Locate every Plasmodium falciparum-infected red blood cell.
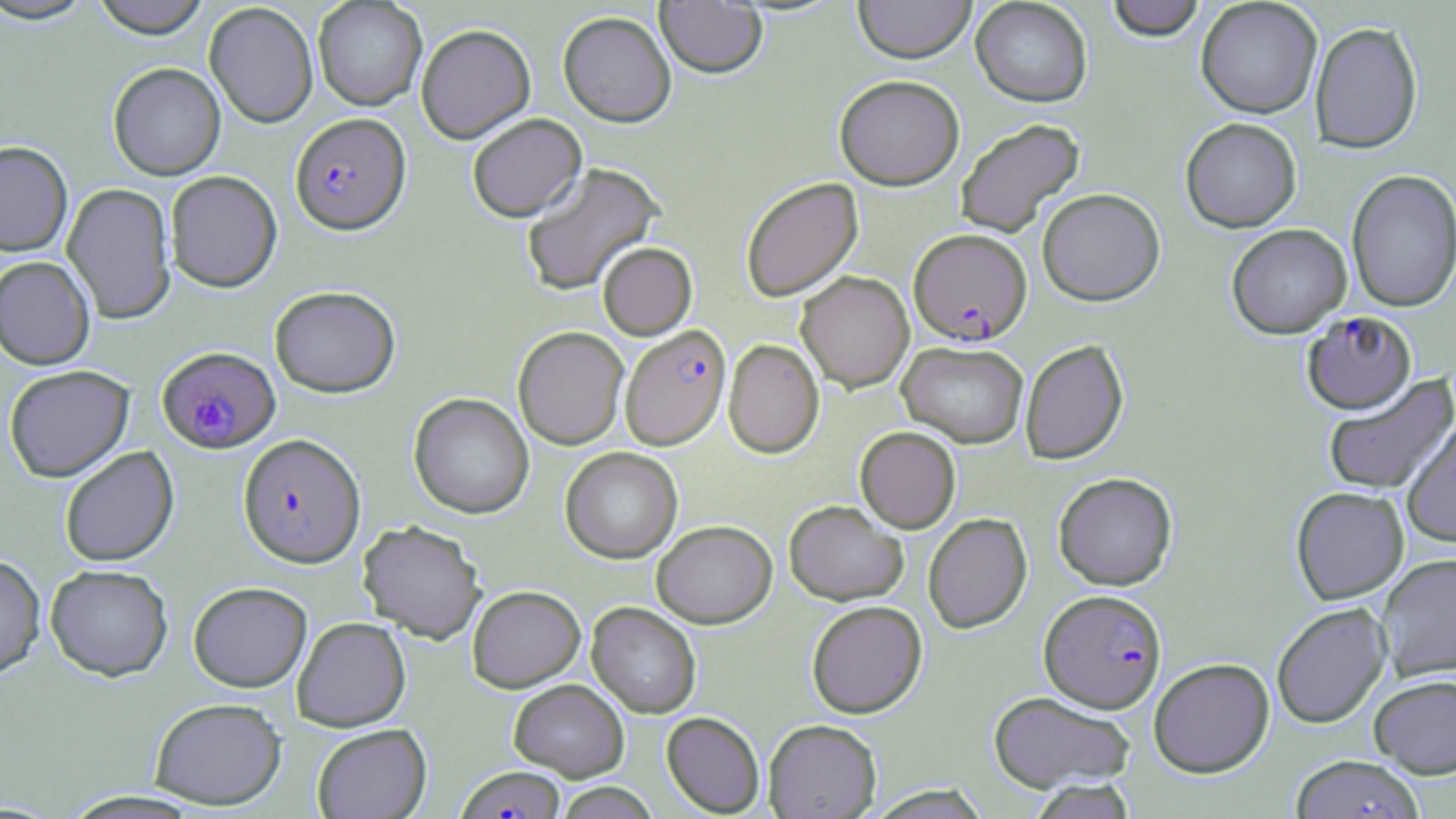

Approximate bounding boxes as [x1, y1, x2, y2] in pixels.
Plasmodium falciparum-infected red blood cells: [290, 112, 410, 234], [909, 228, 1032, 344], [1301, 311, 1417, 414], [619, 324, 731, 450], [157, 346, 280, 453], [238, 433, 365, 567], [1040, 588, 1167, 713], [456, 766, 566, 818].

slide-level diagnosis = Plasmodium falciparum
image size = 1456×819 pixels
preparation = thin blood smear
field of view = single
magnification = 1000x
uninfected red blood cell locations = approximate bounding boxes as [x1, y1, x2, y2] in pixels: [90, 0, 211, 38], [853, 0, 977, 63], [970, 0, 1092, 106], [1105, 0, 1206, 40], [1196, 0, 1322, 118], [0, 1, 98, 24], [313, 1, 427, 110], [655, 1, 767, 78], [204, 2, 318, 128], [557, 10, 676, 127], [1310, 20, 1423, 154], [416, 23, 536, 144], [108, 62, 226, 180], [834, 74, 964, 190], [467, 113, 586, 222], [955, 117, 1085, 238], [1180, 117, 1302, 232], [0, 141, 73, 256], [521, 162, 665, 296], [1346, 169, 1456, 312], [165, 170, 282, 292], [740, 177, 863, 302], [62, 182, 176, 324], [1037, 188, 1165, 305], [1226, 224, 1352, 338], [597, 242, 697, 340], [0, 255, 95, 370], [796, 271, 914, 392], [269, 285, 400, 397], [513, 326, 629, 449], [723, 339, 824, 458], [1020, 339, 1129, 464], [898, 340, 1029, 448], [3, 365, 134, 482], [1323, 374, 1456, 496], [409, 393, 534, 519], [1401, 417, 1456, 547], [855, 426, 961, 532], [59, 446, 179, 567], [560, 447, 683, 562], [1053, 472, 1178, 590], [1290, 486, 1409, 604], [784, 500, 908, 605], [923, 513, 1032, 633], [357, 520, 486, 642], [652, 520, 777, 628], [0, 553, 46, 678], [1376, 553, 1456, 681], [45, 564, 173, 681], [188, 581, 312, 692], [467, 585, 585, 692], [806, 600, 927, 718], [587, 602, 701, 718], [1271, 603, 1391, 729], [292, 616, 411, 731], [1148, 657, 1275, 777], [1369, 674, 1456, 778], [508, 678, 629, 781], [988, 691, 1135, 793], [149, 697, 286, 809], [662, 711, 765, 817], [763, 719, 882, 819], [311, 723, 432, 819], [1290, 754, 1425, 818], [1027, 779, 1138, 819], [553, 782, 661, 818]
modality = light microscopy
stain = May-Grünwald-Giemsa